Outline each blood parasite and name the species.
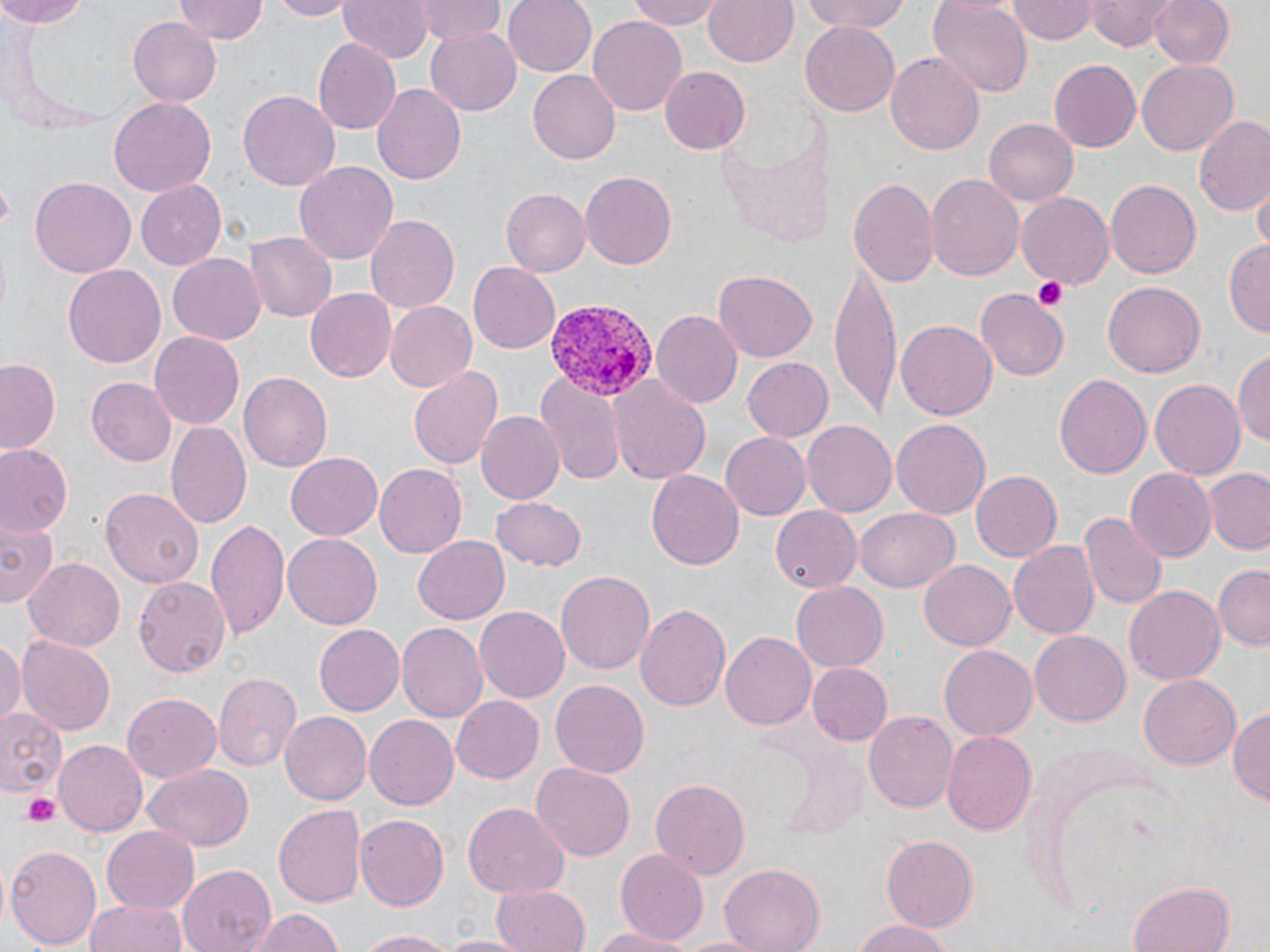
Approximate bounding boxes as named x1/y1/x2/y2 corners in pixels.
Plasmodium vivax-infected red blood cells: (x1=541, y1=299, x2=654, y2=403).
No Plasmodium falciparum, Plasmodium ovale, Plasmodium malariae, Babesia divergens, or Trypanosoma brucei observed.

Summary:
  - Platelet locations: (x1=1032, y1=273, x2=1070, y2=311), (x1=21, y1=793, x2=62, y2=826)
  - Uninfected red blood cell locations: (x1=0, y1=0, x2=94, y2=27), (x1=266, y1=0, x2=356, y2=20), (x1=337, y1=0, x2=432, y2=62), (x1=418, y1=0, x2=505, y2=45), (x1=502, y1=0, x2=595, y2=76), (x1=629, y1=0, x2=726, y2=28), (x1=704, y1=0, x2=798, y2=69), (x1=797, y1=0, x2=913, y2=35), (x1=928, y1=0, x2=1033, y2=96), (x1=1088, y1=0, x2=1174, y2=50), (x1=1150, y1=0, x2=1233, y2=68), (x1=175, y1=1, x2=268, y2=44), (x1=1008, y1=2, x2=1099, y2=44), (x1=588, y1=14, x2=688, y2=114), (x1=127, y1=17, x2=222, y2=106), (x1=802, y1=24, x2=900, y2=116), (x1=425, y1=27, x2=524, y2=115), (x1=313, y1=37, x2=400, y2=133), (x1=886, y1=50, x2=986, y2=156), (x1=1050, y1=59, x2=1141, y2=152), (x1=1137, y1=60, x2=1237, y2=156), (x1=659, y1=66, x2=751, y2=155), (x1=528, y1=70, x2=619, y2=165), (x1=372, y1=83, x2=467, y2=186), (x1=239, y1=90, x2=340, y2=191), (x1=108, y1=97, x2=216, y2=195), (x1=1195, y1=116, x2=1270, y2=219), (x1=984, y1=117, x2=1079, y2=207), (x1=294, y1=160, x2=400, y2=266), (x1=579, y1=168, x2=676, y2=266), (x1=926, y1=172, x2=1024, y2=281), (x1=851, y1=173, x2=939, y2=291), (x1=31, y1=177, x2=136, y2=277), (x1=136, y1=179, x2=227, y2=268), (x1=1105, y1=179, x2=1200, y2=279), (x1=1252, y1=183, x2=1270, y2=253), (x1=500, y1=187, x2=590, y2=276), (x1=1017, y1=193, x2=1115, y2=288), (x1=365, y1=215, x2=463, y2=313), (x1=244, y1=231, x2=336, y2=322), (x1=1224, y1=241, x2=1270, y2=336), (x1=167, y1=252, x2=265, y2=341), (x1=831, y1=261, x2=900, y2=420), (x1=470, y1=262, x2=559, y2=353), (x1=64, y1=265, x2=166, y2=368), (x1=710, y1=270, x2=817, y2=363), (x1=1102, y1=282, x2=1203, y2=379), (x1=305, y1=289, x2=397, y2=382), (x1=977, y1=292, x2=1066, y2=378), (x1=385, y1=301, x2=478, y2=393), (x1=652, y1=310, x2=744, y2=408), (x1=896, y1=319, x2=996, y2=420), (x1=150, y1=330, x2=245, y2=431), (x1=1233, y1=351, x2=1270, y2=448), (x1=741, y1=356, x2=833, y2=441), (x1=0, y1=357, x2=63, y2=454), (x1=408, y1=364, x2=502, y2=471), (x1=240, y1=372, x2=335, y2=473), (x1=538, y1=373, x2=625, y2=481), (x1=1054, y1=373, x2=1152, y2=480), (x1=86, y1=376, x2=178, y2=467), (x1=610, y1=377, x2=711, y2=482), (x1=1150, y1=377, x2=1244, y2=478), (x1=487, y1=385, x2=607, y2=496), (x1=475, y1=411, x2=562, y2=504), (x1=165, y1=418, x2=251, y2=530), (x1=893, y1=418, x2=990, y2=520), (x1=801, y1=421, x2=896, y2=518), (x1=721, y1=431, x2=810, y2=520), (x1=0, y1=444, x2=73, y2=537), (x1=286, y1=451, x2=385, y2=540), (x1=375, y1=463, x2=467, y2=556), (x1=1124, y1=467, x2=1215, y2=562), (x1=969, y1=469, x2=1061, y2=562), (x1=1204, y1=469, x2=1270, y2=553), (x1=645, y1=470, x2=744, y2=570), (x1=102, y1=487, x2=204, y2=586), (x1=489, y1=496, x2=586, y2=571), (x1=771, y1=506, x2=861, y2=591), (x1=853, y1=508, x2=958, y2=592), (x1=1080, y1=514, x2=1164, y2=609), (x1=206, y1=516, x2=292, y2=643), (x1=0, y1=520, x2=60, y2=609), (x1=283, y1=532, x2=384, y2=629), (x1=413, y1=535, x2=512, y2=624), (x1=1008, y1=541, x2=1099, y2=639), (x1=25, y1=557, x2=125, y2=651), (x1=919, y1=559, x2=1016, y2=650), (x1=1213, y1=566, x2=1269, y2=650), (x1=555, y1=570, x2=655, y2=674), (x1=135, y1=575, x2=231, y2=676), (x1=791, y1=581, x2=889, y2=671), (x1=1123, y1=584, x2=1226, y2=684), (x1=636, y1=603, x2=733, y2=715), (x1=474, y1=606, x2=570, y2=702), (x1=397, y1=621, x2=489, y2=722), (x1=315, y1=625, x2=403, y2=716), (x1=720, y1=630, x2=816, y2=731), (x1=1029, y1=631, x2=1131, y2=726), (x1=0, y1=636, x2=24, y2=725), (x1=16, y1=636, x2=117, y2=735), (x1=940, y1=646, x2=1036, y2=739), (x1=806, y1=661, x2=893, y2=746), (x1=213, y1=672, x2=301, y2=771), (x1=1139, y1=673, x2=1241, y2=770), (x1=549, y1=679, x2=649, y2=779), (x1=122, y1=691, x2=222, y2=783), (x1=451, y1=695, x2=545, y2=783), (x1=0, y1=703, x2=66, y2=800), (x1=863, y1=707, x2=958, y2=811), (x1=1230, y1=707, x2=1270, y2=811), (x1=279, y1=711, x2=371, y2=806), (x1=365, y1=713, x2=458, y2=810), (x1=941, y1=728, x2=1037, y2=837), (x1=55, y1=740, x2=148, y2=838), (x1=531, y1=760, x2=634, y2=860), (x1=142, y1=766, x2=253, y2=851), (x1=650, y1=777, x2=752, y2=878), (x1=462, y1=802, x2=567, y2=899), (x1=274, y1=804, x2=367, y2=909), (x1=356, y1=814, x2=449, y2=909), (x1=101, y1=826, x2=200, y2=915), (x1=881, y1=835, x2=976, y2=933), (x1=6, y1=843, x2=101, y2=952), (x1=614, y1=849, x2=709, y2=943), (x1=720, y1=863, x2=824, y2=952), (x1=177, y1=864, x2=274, y2=952), (x1=1131, y1=879, x2=1236, y2=952), (x1=489, y1=884, x2=590, y2=952), (x1=87, y1=898, x2=189, y2=952), (x1=249, y1=908, x2=345, y2=951), (x1=850, y1=918, x2=954, y2=952), (x1=593, y1=927, x2=692, y2=951), (x1=357, y1=929, x2=455, y2=951), (x1=438, y1=934, x2=533, y2=952), (x1=670, y1=934, x2=771, y2=951)
  - Slide-level diagnosis: Plasmodium vivax
  - Magnification: 1000x
  - Field of view: single
  - Image size: 1270×952 pixels
  - Preparation: thin blood film
  - Modality: optical microscopy
  - Stain: May-Grünwald-Giemsa